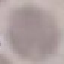

Result: no malaria parasites detected. Cell patch, automatically extracted from a larger field of view and resized to 64 × 64 pixels. Giemsa-stained preparation. Thin smear of blood. Photographed with a smartphone camera at the microscope eyepiece.